Evaluate for malaria.
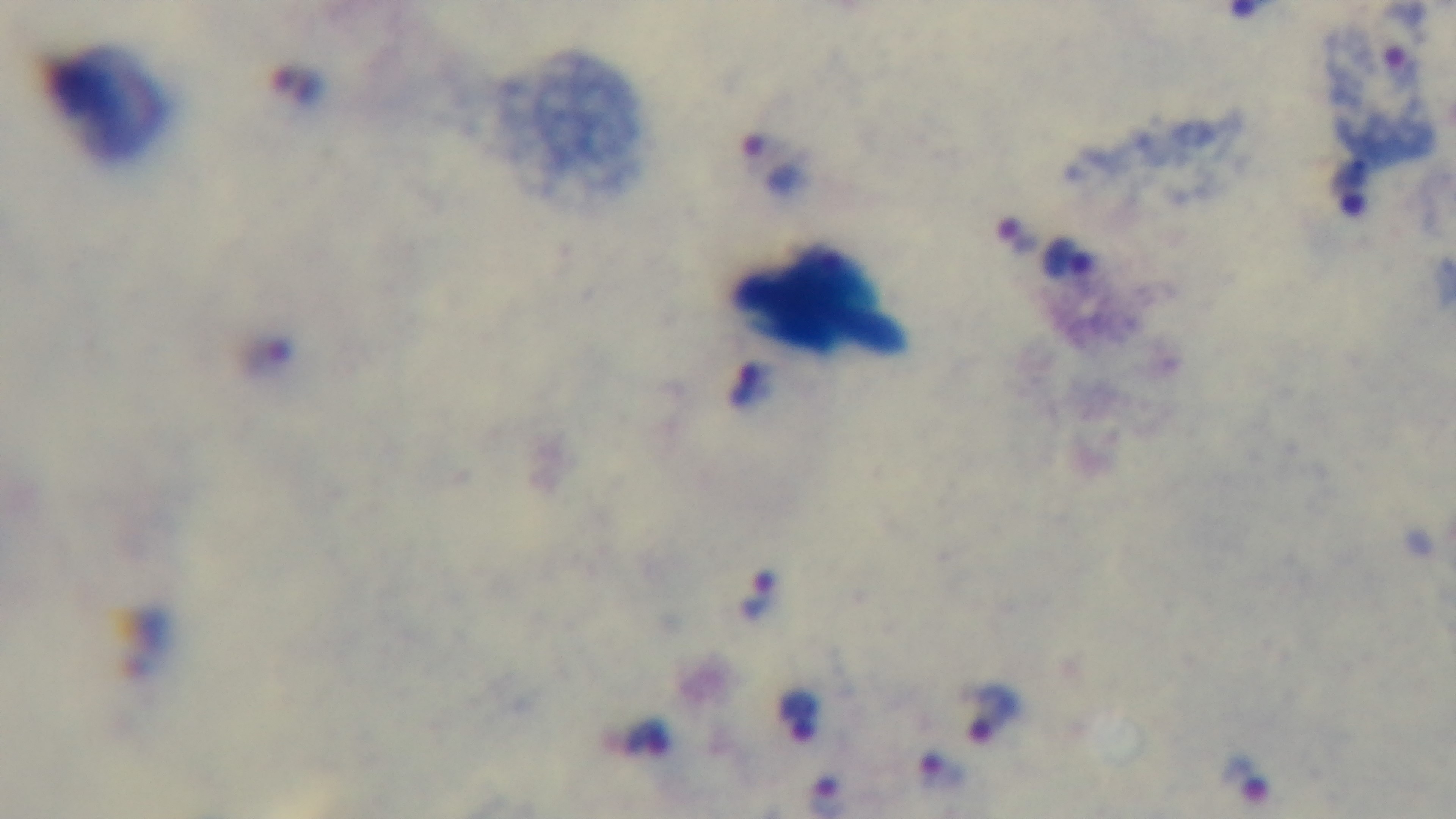

Infected.

Giemsa-stained. One field from the slide. Preparation: thick smear. Mounted 4K digital camera. Light microscopy. Oil-immersion objective, 100x.